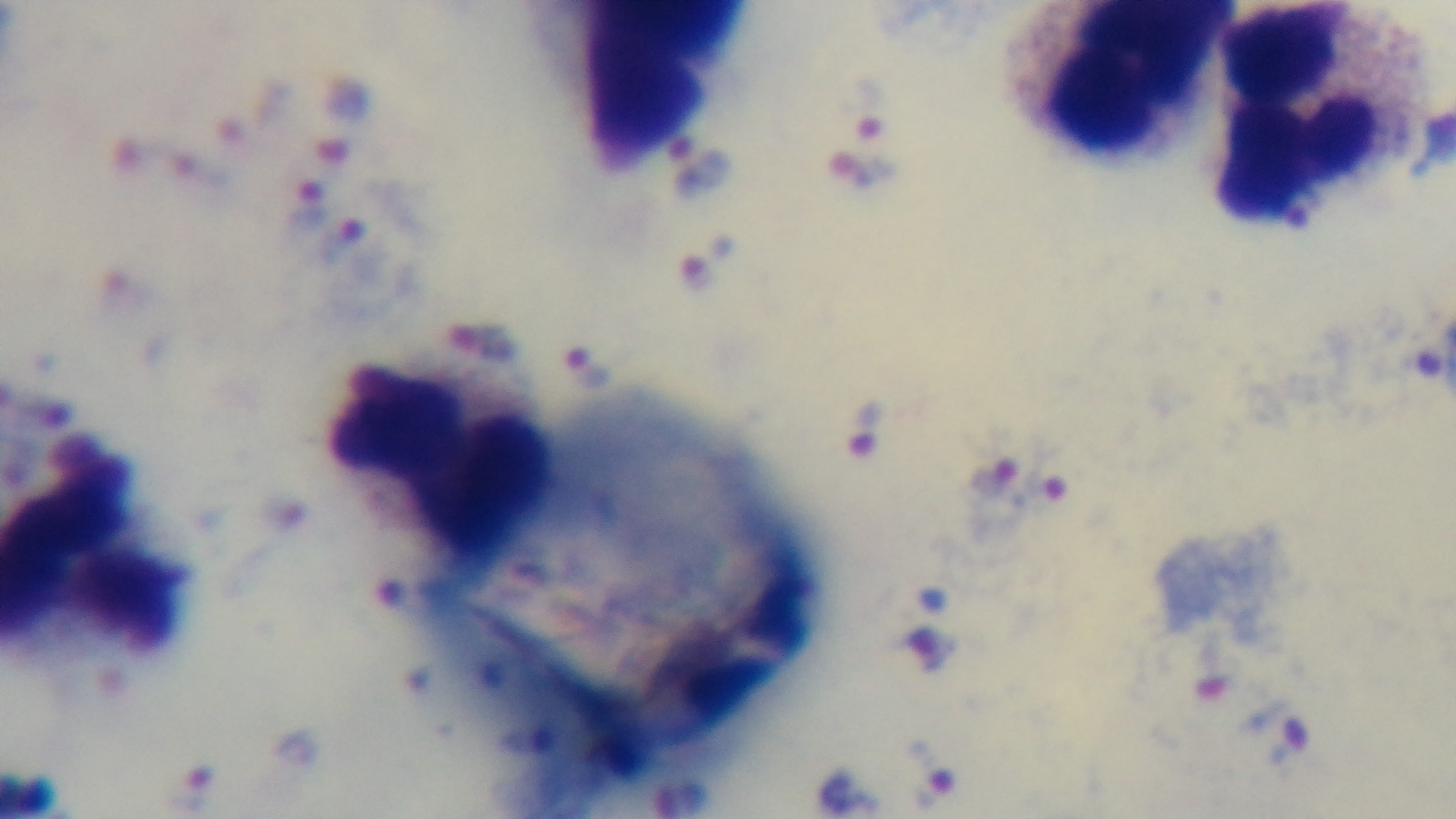
capture = mounted 4K digital camera
field of view = one from the slide
preparation = thick blood film
stain = Giemsa
modality = light microscopy
malaria status = infected
objective = 100x oil immersion